Report the malaria status of this cell.
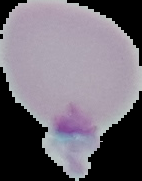
Uninfected.

image_size: 142×181 pixels
preparation: thin blood film
image_type: cell region segmented out of the field of view; surrounding area masked to black